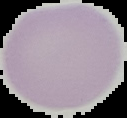

image size = 127×118 pixels
image type = segmented cell region on a black background
preparation = thin blood film
result = no malaria parasites detected